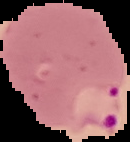
Image is 130×142 pixels. Segmented cell region on a black background. From a thin blood smear. Malaria status: parasitized.